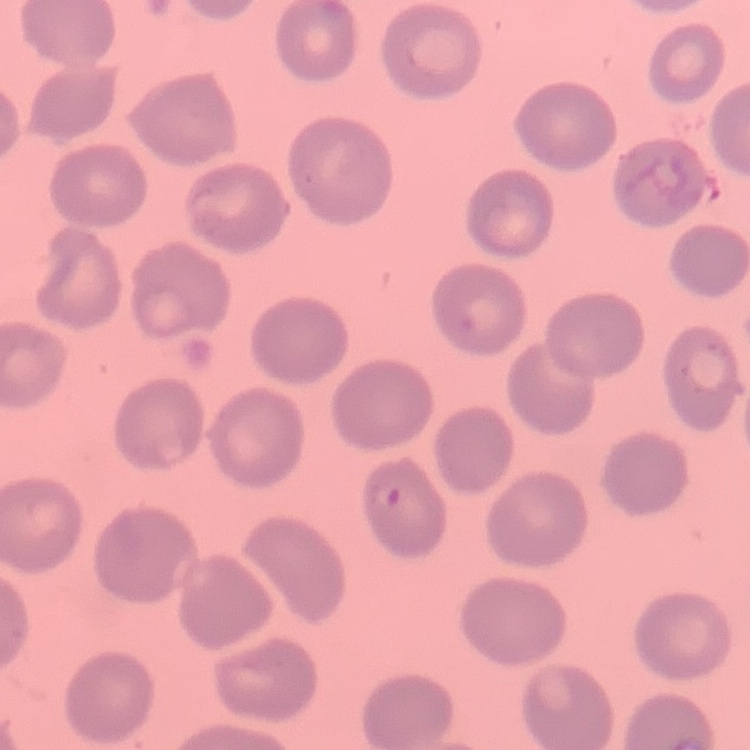
red blood cell morphology = no rouleaux formation
image type = square crop of a larger photomicrograph
preparation = thin blood film
stain = Field's or Giemsa